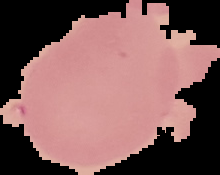
Summary:
  - Malaria status: uninfected
  - Image size: 220×175 pixels
  - Image type: segmented cell region on a black background
  - Preparation: thin blood film